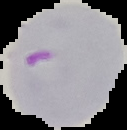
preparation = thin blood smear
image type = segmented cell region on a black background
malaria status = parasitized
image size = 127×130 pixels